Draw a bounding box around every malaria parasite.
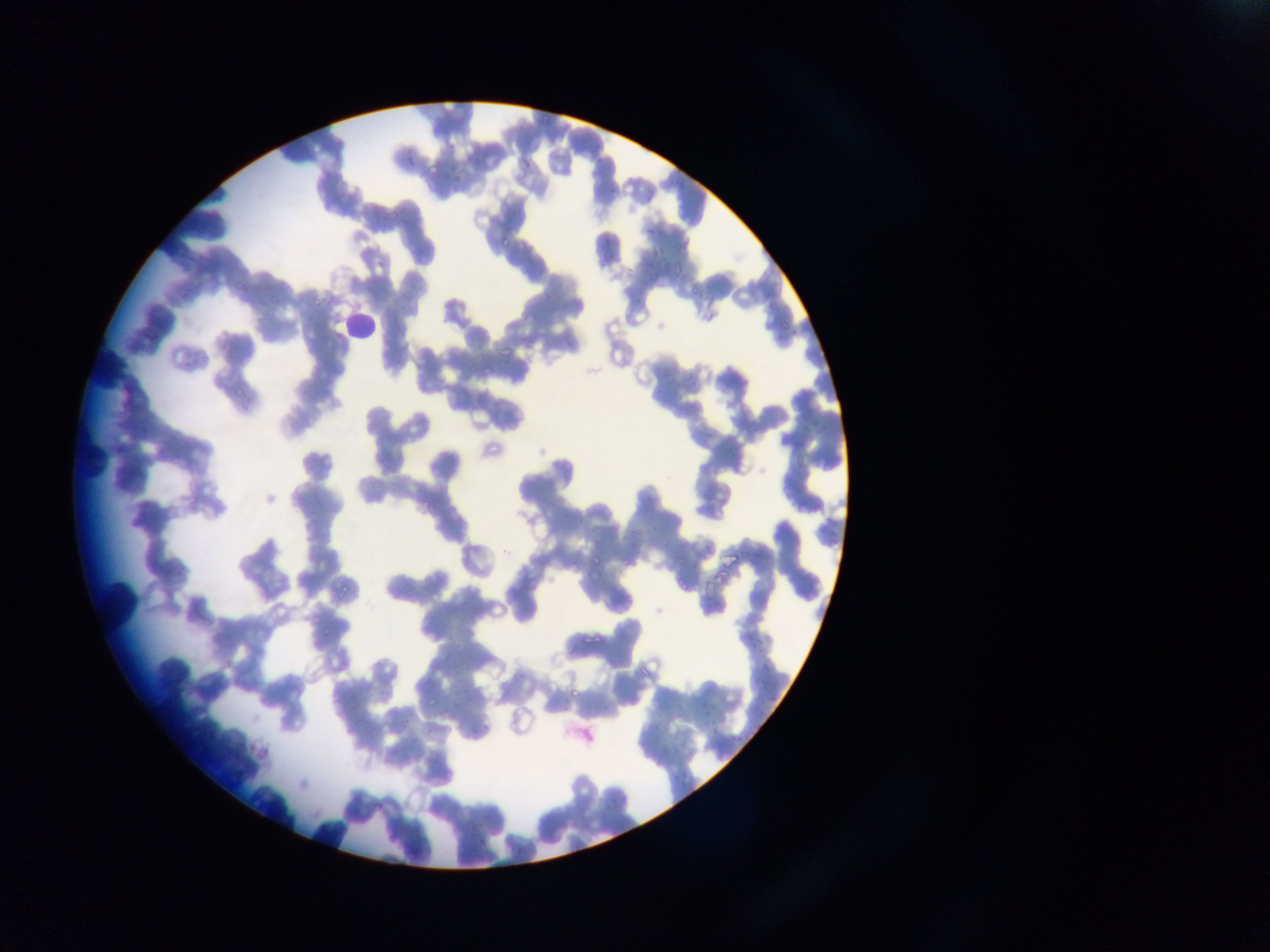
Approximate bounding boxes as {left, top, right, bottom} in pixels.
Malaria parasites: {538, 113, 552, 127}, {403, 151, 421, 169}, {466, 152, 482, 167}, {518, 154, 533, 173}, {424, 166, 443, 176}, {448, 173, 466, 190}, {638, 224, 664, 240}, {499, 232, 513, 250}, {598, 234, 612, 252}, {646, 243, 667, 256}, {671, 265, 685, 279}, {230, 277, 252, 292}, {264, 293, 285, 306}, {312, 294, 325, 308}, {778, 315, 794, 330}, {472, 328, 490, 339}, {496, 340, 519, 355}, {477, 361, 503, 379}, {227, 388, 250, 401}, {791, 452, 806, 465}, {184, 492, 202, 506}, {587, 552, 605, 573}, {672, 577, 688, 594}, {333, 585, 354, 603}, {307, 614, 325, 627}, {579, 626, 601, 644}, {744, 629, 763, 651}, {317, 632, 329, 640}, {634, 663, 653, 678}, {760, 663, 774, 676}, {748, 680, 757, 686}, {452, 681, 472, 699}, {568, 686, 583, 704}, {694, 696, 717, 714}, {439, 704, 450, 718}, {396, 718, 411, 732}, {705, 718, 725, 742}, {468, 721, 489, 736}, {729, 732, 743, 745}, {385, 747, 397, 758}, {222, 760, 246, 781}, {669, 769, 687, 784}, {366, 795, 386, 815}, {457, 818, 473, 831}, {476, 836, 492, 852}.

leukocyte locations = approximate bounding boxes as {left, top, right, bottom} in pixels: {343, 314, 378, 348}
preparation = thin blood smear
capture = mobile-phone photograph through a microscope
field of view = single
image size = 1270×952 pixels
country = Ghana